Assess this cell for malaria.
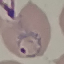
It is parasitized.

capture: smartphone camera at the microscope eyepiece
image_type: automatically extracted cell patch, resized to 64 × 64 pixels
stain: Giemsa
preparation: thin blood film